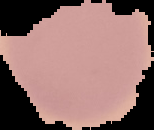
Summary:
  - Image type: cell region segmented out of the field of view; surrounding area masked to black
  - Result: no malaria parasites seen
  - Image size: 154×130 pixels
  - Preparation: thin blood film